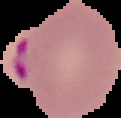
image size = 121×118 pixels
result = Plasmodium parasites identified
preparation = thin blood smear
image type = segmented cell region on a black background